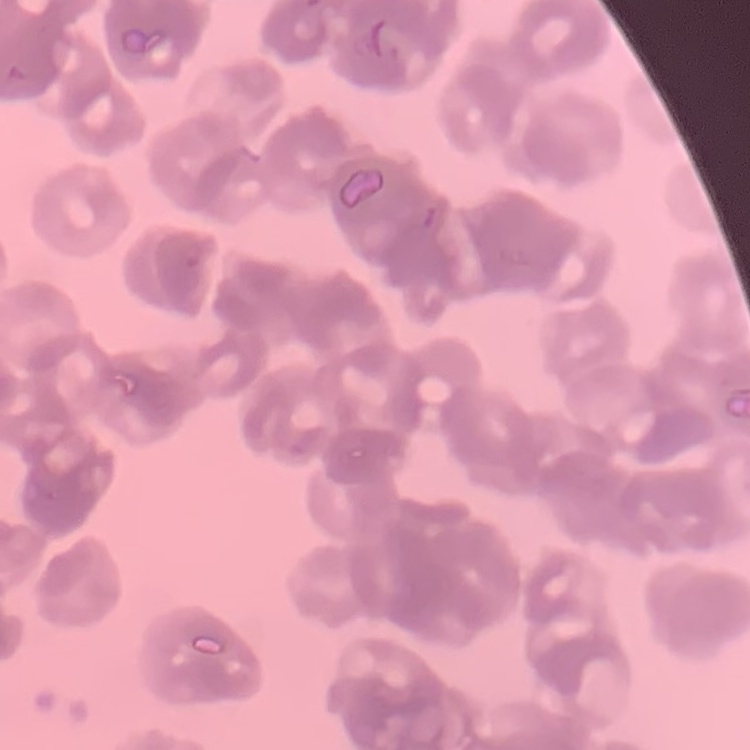

erythrocyte morphology = rouleaux formation
preparation = thin peripheral smear
stain = Field's or Giemsa
image type = one tile cut from a larger photomicrograph